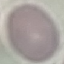

{
  "malaria_status": "uninfected",
  "stain": "Giemsa",
  "preparation": "thin smear",
  "capture": "smartphone through the microscope eyepiece",
  "image_type": "cell patch, automatically extracted from a larger field of view and resized to 64 × 64 pixels"
}